Evaluate for malaria.
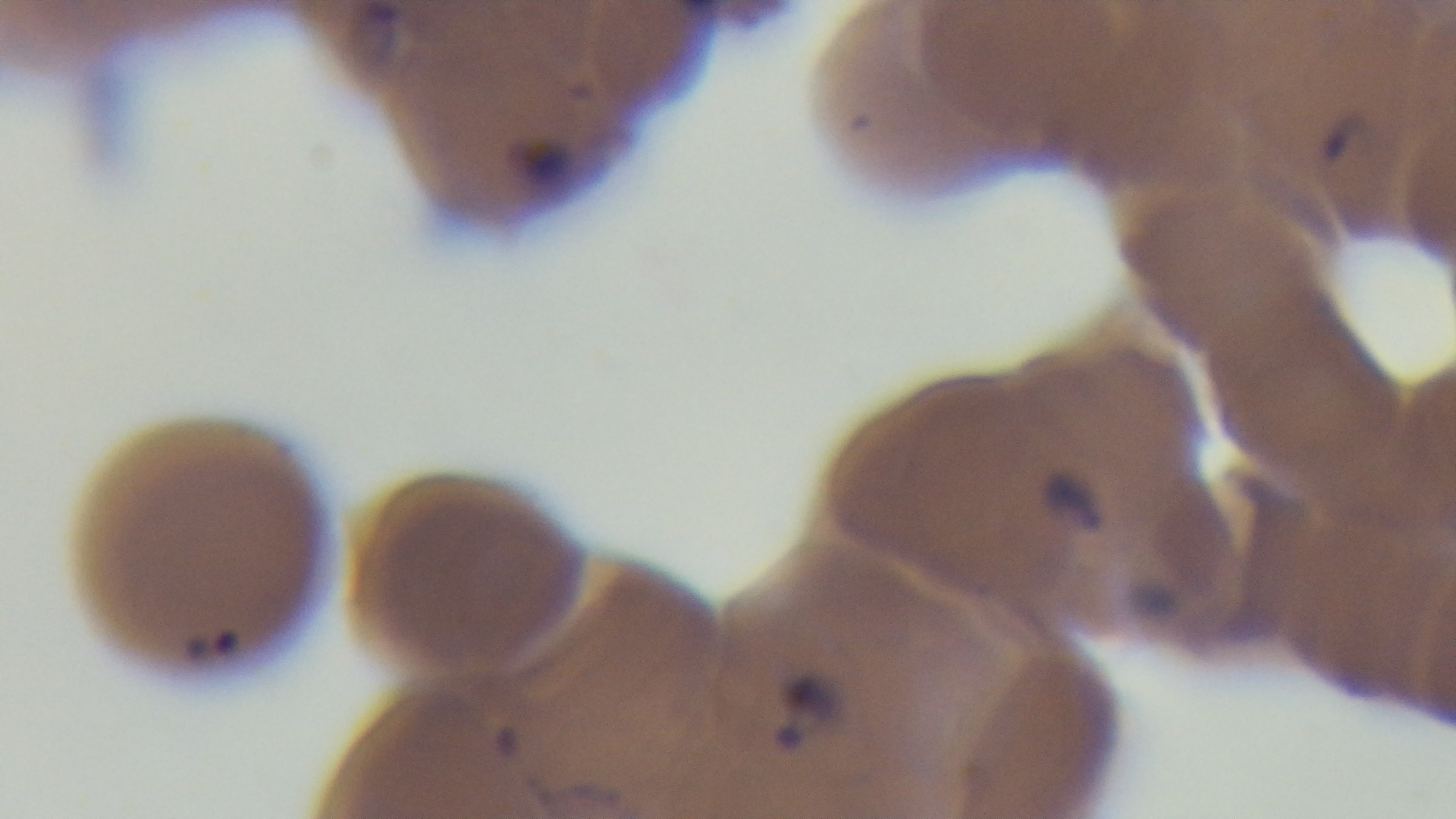
Positive.

field_of_view: one from the slide
objective: 100x oil immersion
stain: Giemsa
capture: mounted 4K digital camera
modality: light microscopy
preparation: thin blood film